Locate malaria parasites and identify their life-cycle stages.
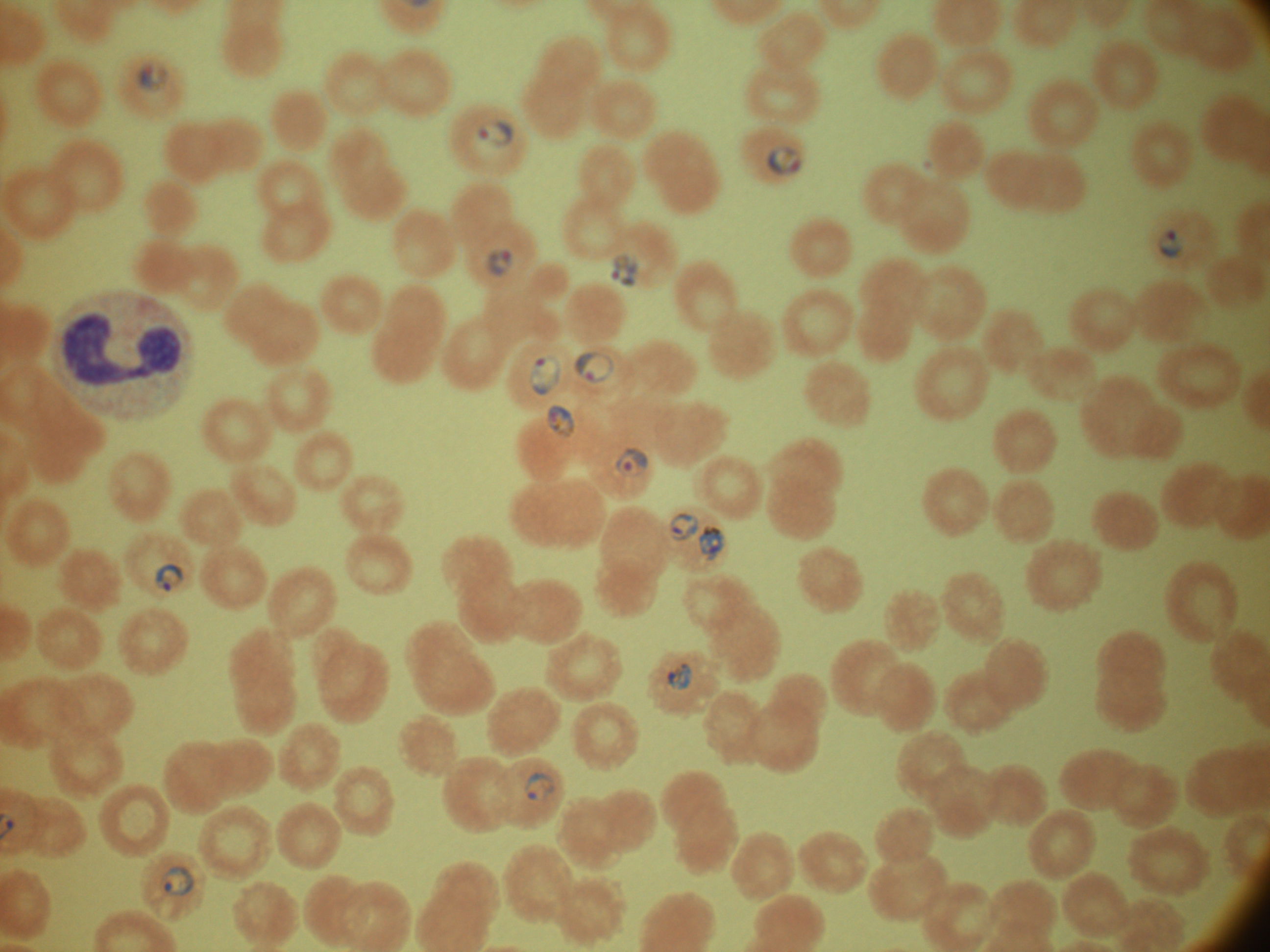
Approximate bounding boxes as (x1, y1, x2, y2) in pixels, from the source annotation, which is not necessarily exhaustive.
Ring forms: (135, 61, 165, 95), (477, 119, 513, 146), (767, 146, 801, 176), (1156, 228, 1186, 259), (487, 248, 515, 277), (611, 254, 638, 288), (573, 351, 613, 384), (531, 355, 561, 394), (549, 405, 575, 438), (615, 447, 648, 477), (667, 512, 699, 542), (699, 526, 724, 561), (154, 563, 184, 592), (666, 663, 693, 690), (524, 772, 555, 802), (160, 867, 194, 896).

Image is 1270×952 pixels. Giemsa-stained preparation. Acquired with a Leica DM2000 optical microscope and its built-in camera. Thin blood smear. Captured at 100x magnification. Species: Plasmodium falciparum. One field from this slide.